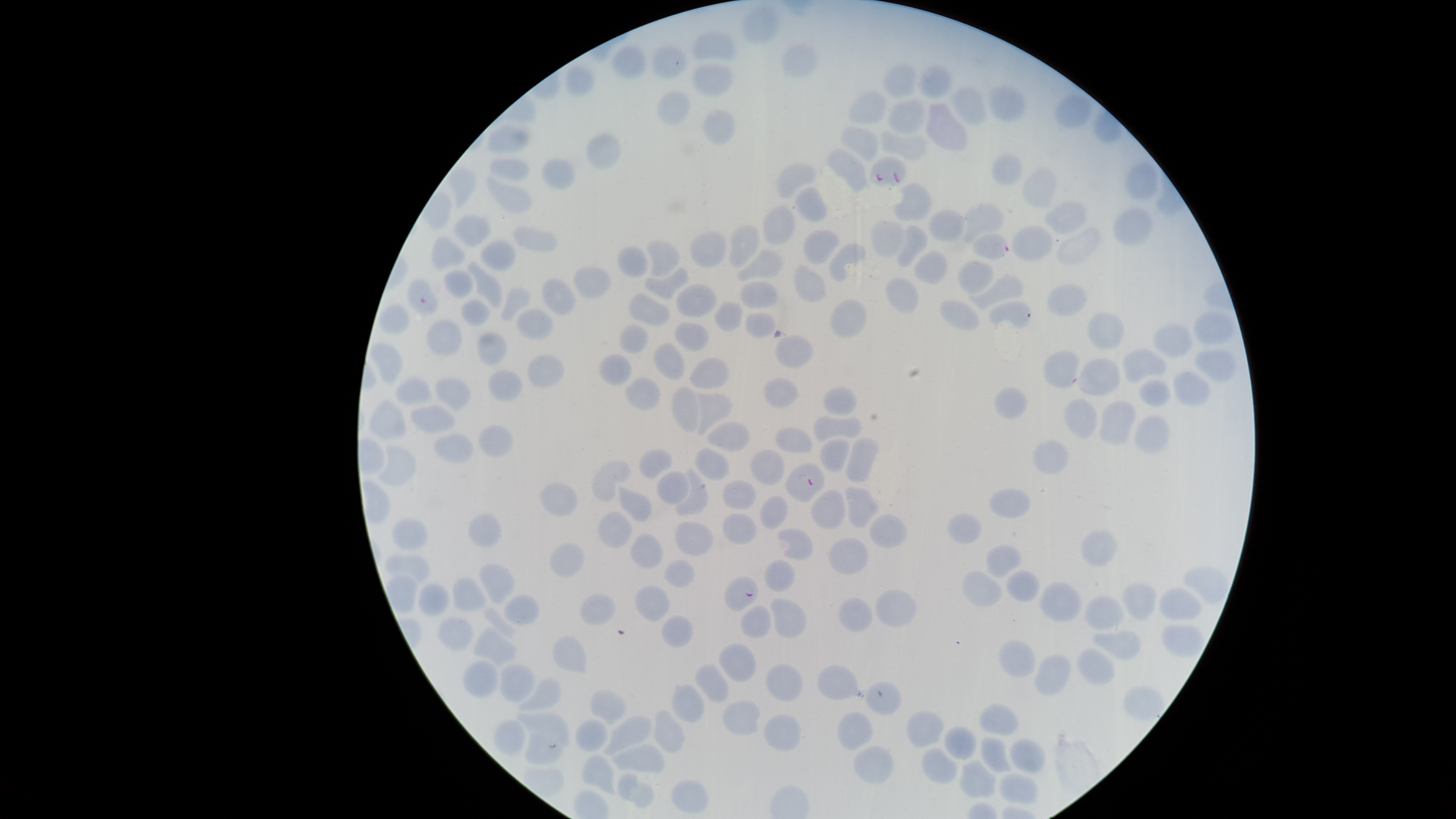
capture: smartphone photograph through the microscope eyepiece
preparation: thin smear of blood
stain: Giemsa
image_size: 1456×819 pixels
presence: malaria parasites detected
species: Plasmodium falciparum
field_of_view: single
visible_region: circular
uninfected_RBCs: 'approximate bounding boxes as (left, top, right, bottom) in pixels: (741, 6, 779, 43), (692, 31, 737, 61), (781, 43, 819, 78), (612, 44, 648, 79), (651, 44, 688, 79), (691, 61, 736, 97), (566, 64, 594, 98), (882, 64, 917, 100), (919, 64, 953, 97), (987, 83, 1026, 119), (950, 85, 987, 125), (848, 89, 887, 126), (657, 90, 691, 125), (1054, 93, 1092, 129), (886, 98, 927, 135), (925, 101, 968, 151), (703, 108, 736, 144), (488, 124, 530, 154), (840, 126, 880, 162), (880, 129, 929, 162), (586, 132, 623, 170), (825, 146, 868, 192), (990, 152, 1023, 185), (489, 157, 529, 181), (542, 158, 575, 190), (1124, 160, 1159, 202), (775, 162, 817, 199), (447, 166, 477, 212), (1021, 167, 1059, 207), (485, 174, 532, 214), (893, 182, 932, 222), (794, 187, 828, 222), (1043, 200, 1087, 234), (965, 203, 1004, 243), (762, 205, 796, 245), (1113, 205, 1153, 248), (929, 209, 965, 242), (453, 214, 490, 247), (871, 219, 905, 258), (728, 224, 760, 269), (896, 225, 928, 268), (1011, 225, 1054, 262), (513, 226, 558, 252), (1057, 226, 1102, 265), (803, 229, 840, 265), (689, 230, 727, 269), (431, 235, 466, 271), (479, 239, 516, 271), (646, 240, 680, 278), (828, 243, 867, 282), (618, 245, 648, 277), (736, 248, 783, 281), (913, 250, 948, 284), (957, 259, 994, 294), (466, 261, 502, 309), (794, 264, 827, 302), (572, 265, 612, 299), (644, 266, 689, 300), (443, 269, 475, 298), (968, 274, 1024, 314), (406, 277, 438, 315), (542, 277, 576, 316), (885, 277, 919, 313), (739, 281, 778, 309), (676, 283, 716, 318), (1047, 284, 1088, 315), (500, 286, 531, 321), (628, 293, 671, 326), (460, 298, 491, 326), (830, 299, 867, 338), (939, 299, 981, 332), (988, 300, 1032, 329), (713, 301, 743, 332), (378, 303, 410, 334), (515, 308, 555, 338), (1193, 310, 1235, 345), (1087, 311, 1125, 351), (745, 312, 777, 338), (426, 318, 463, 354), (674, 321, 709, 351), (1152, 322, 1193, 357), (619, 323, 649, 354), (476, 331, 508, 365), (774, 334, 814, 369), (369, 342, 404, 384), (654, 342, 686, 380), (1121, 348, 1166, 384), (1194, 348, 1238, 383), (1042, 349, 1080, 388), (527, 353, 565, 388), (598, 353, 632, 385), (689, 357, 730, 390), (1076, 358, 1121, 395), (489, 369, 524, 401), (1172, 370, 1211, 408), (434, 376, 471, 414), (624, 377, 660, 411), (763, 377, 799, 407), (396, 378, 433, 405), (1137, 378, 1171, 407), (671, 385, 700, 433), (822, 386, 857, 416), (993, 386, 1028, 420), (695, 391, 733, 436), (1063, 398, 1097, 439), (369, 399, 407, 439), (1099, 400, 1136, 445), (409, 404, 456, 433), (813, 414, 861, 442), (1133, 415, 1170, 455), (707, 420, 751, 451), (477, 424, 515, 457), (775, 426, 812, 453), (432, 433, 475, 464), (845, 436, 880, 483), (819, 437, 850, 472), (1032, 439, 1069, 475), (377, 443, 417, 486), (694, 447, 730, 480), (638, 448, 673, 479), (750, 448, 786, 484), (592, 460, 631, 503), (674, 468, 709, 516), (655, 471, 690, 504), (723, 480, 756, 509), (539, 482, 578, 517), (617, 485, 652, 522), (845, 485, 880, 530), (988, 488, 1032, 518), (811, 490, 846, 530), (759, 495, 788, 529), (597, 511, 632, 548), (947, 512, 983, 544), (468, 513, 502, 547), (722, 513, 756, 546), (870, 514, 908, 548), (392, 518, 428, 551), (673, 521, 714, 556), (777, 528, 814, 560), (1081, 530, 1117, 566), (629, 534, 664, 568), (828, 537, 868, 575), (549, 542, 584, 577), (986, 544, 1021, 578), (384, 554, 430, 582), (663, 558, 695, 587), (763, 558, 796, 592), (478, 563, 516, 604), (1006, 569, 1040, 602), (962, 570, 1002, 608), (452, 576, 487, 611), (1039, 579, 1083, 623), (1122, 582, 1158, 620), (417, 583, 449, 617), (635, 585, 670, 623), (1159, 587, 1202, 620), (875, 588, 916, 627), (579, 593, 616, 625), (503, 594, 540, 625), (1084, 595, 1125, 629), (769, 597, 807, 638), (838, 597, 873, 633), (740, 605, 771, 639), (480, 608, 517, 640), (660, 615, 694, 647), (437, 617, 474, 650), (1161, 623, 1205, 657), (473, 627, 518, 667), (1092, 630, 1140, 660), (551, 635, 588, 673), (997, 639, 1035, 678), (718, 642, 757, 682), (1077, 648, 1115, 686), (1034, 653, 1071, 695), (462, 662, 499, 698), (694, 662, 731, 702), (764, 662, 803, 702), (498, 663, 535, 703), (816, 664, 859, 699), (517, 677, 562, 711), (865, 681, 902, 715), (671, 683, 705, 723), (590, 688, 628, 724), (722, 700, 760, 735), (978, 704, 1018, 736), (652, 709, 685, 752), (906, 710, 945, 747), (837, 711, 872, 750), (515, 712, 570, 746), (763, 713, 801, 751), (603, 716, 652, 756), (494, 719, 526, 757), (575, 719, 608, 753), (943, 726, 977, 759), (523, 731, 563, 766), (980, 737, 1012, 773), (1010, 738, 1047, 774), (612, 744, 665, 773), (853, 744, 893, 784), (921, 746, 958, 784), (581, 754, 618, 795), (959, 759, 997, 799), (617, 773, 656, 808), (999, 773, 1037, 804), (670, 780, 708, 814)'
parasitized_RBCs: 'approximate bounding boxes as (left, top, right, bottom) in pixels: (869, 156, 908, 186), (972, 233, 1009, 259), (784, 461, 824, 503), (723, 575, 758, 611)'